Outline each uninfected red blood cell.
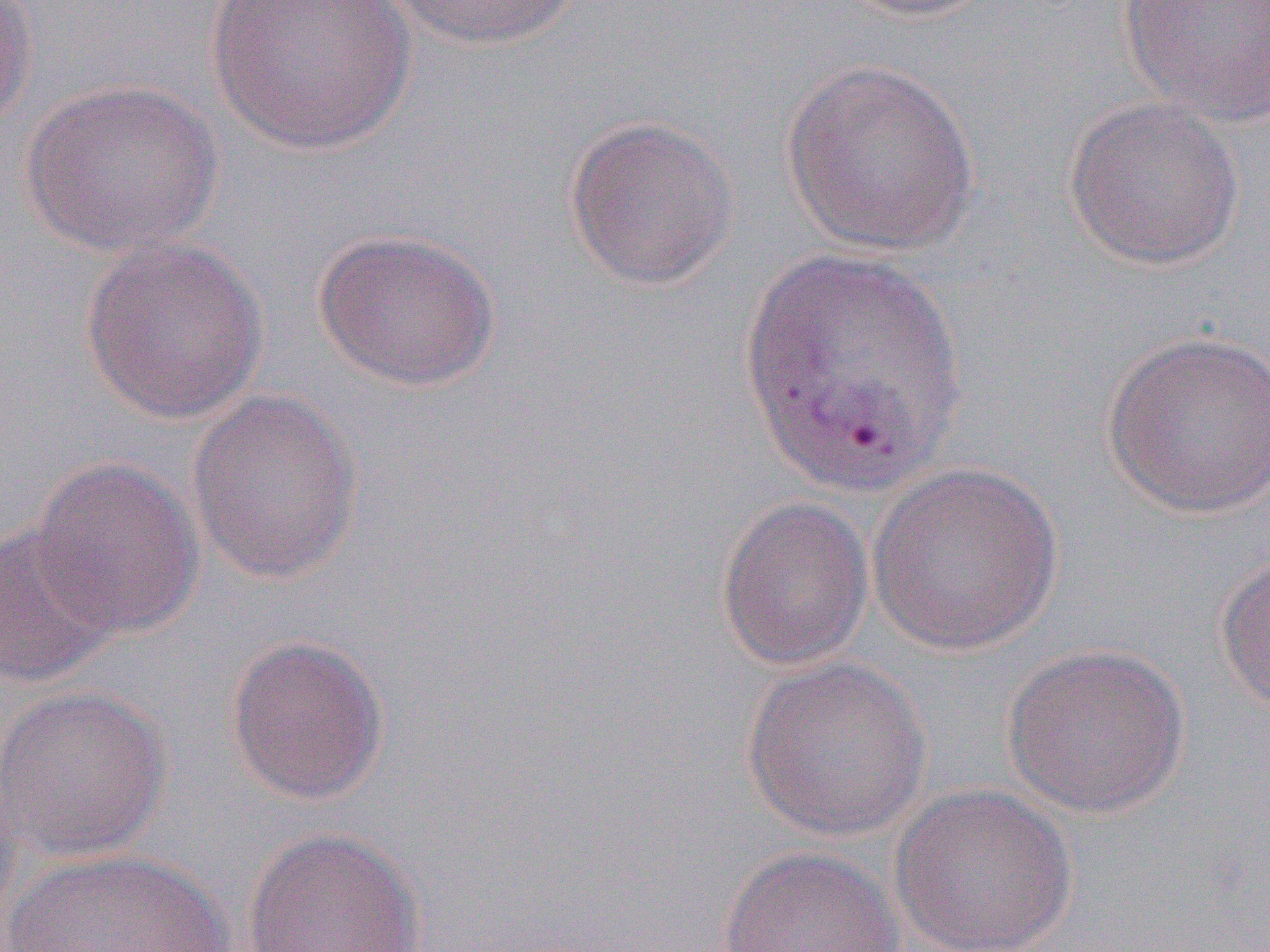

Approximate bounding boxes as named x1/y1/x2/y2 corners in pixels.
Uninfected red blood cells: (x1=0, y1=0, x2=40, y2=138), (x1=205, y1=0, x2=415, y2=156), (x1=385, y1=0, x2=582, y2=51), (x1=829, y1=0, x2=1002, y2=23), (x1=1117, y1=0, x2=1270, y2=127), (x1=779, y1=58, x2=982, y2=257), (x1=19, y1=79, x2=224, y2=258), (x1=1063, y1=97, x2=1245, y2=271), (x1=562, y1=115, x2=740, y2=291), (x1=313, y1=227, x2=500, y2=393), (x1=79, y1=234, x2=270, y2=425), (x1=736, y1=245, x2=973, y2=501), (x1=1101, y1=330, x2=1270, y2=518), (x1=186, y1=389, x2=365, y2=585), (x1=29, y1=456, x2=205, y2=640), (x1=867, y1=463, x2=1064, y2=657), (x1=715, y1=495, x2=874, y2=672), (x1=0, y1=522, x2=122, y2=688), (x1=1214, y1=553, x2=1270, y2=720), (x1=224, y1=634, x2=391, y2=806), (x1=1000, y1=643, x2=1192, y2=820), (x1=740, y1=656, x2=932, y2=843), (x1=0, y1=685, x2=173, y2=862), (x1=0, y1=777, x2=23, y2=947), (x1=889, y1=783, x2=1078, y2=952), (x1=242, y1=826, x2=428, y2=952), (x1=717, y1=846, x2=905, y2=952), (x1=5, y1=848, x2=238, y2=952).

Slide-level diagnosis: Plasmodium vivax. Thin blood film. 1000x magnification. Image is 1270×952 pixels. One field of a larger specimen. Light microscopy.